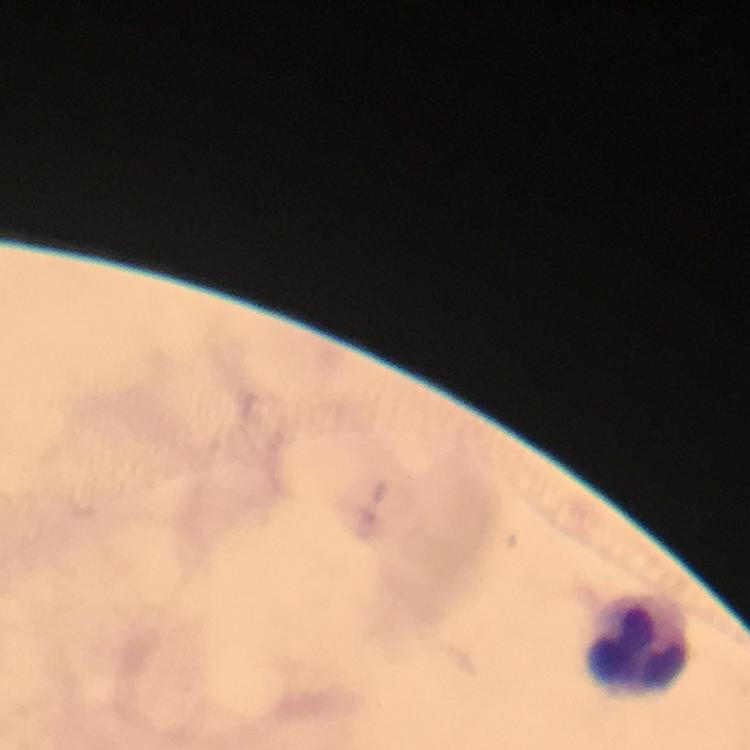
Approximate centers as (x, y) in pixels. Leukocyte locations: (637, 639). Giemsa-stained preparation. Image is 750×750 pixels. Malaria parasites: none seen. A crop from one field of view. From a diagnostic examination for malaria. 100x magnification. Immersion oil was used. Photographed with a smartphone mounted on the microscope. Thick blood smear.